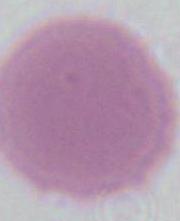

Summary:
  - Modality: micrograph
  - Magnification: 1000x
  - Identification: erythrocyte